Identify the parasite.
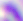

This is Toxoplasma gondii.

modality = micrograph
magnification = 400x